Outline each uninfected red blood cell.
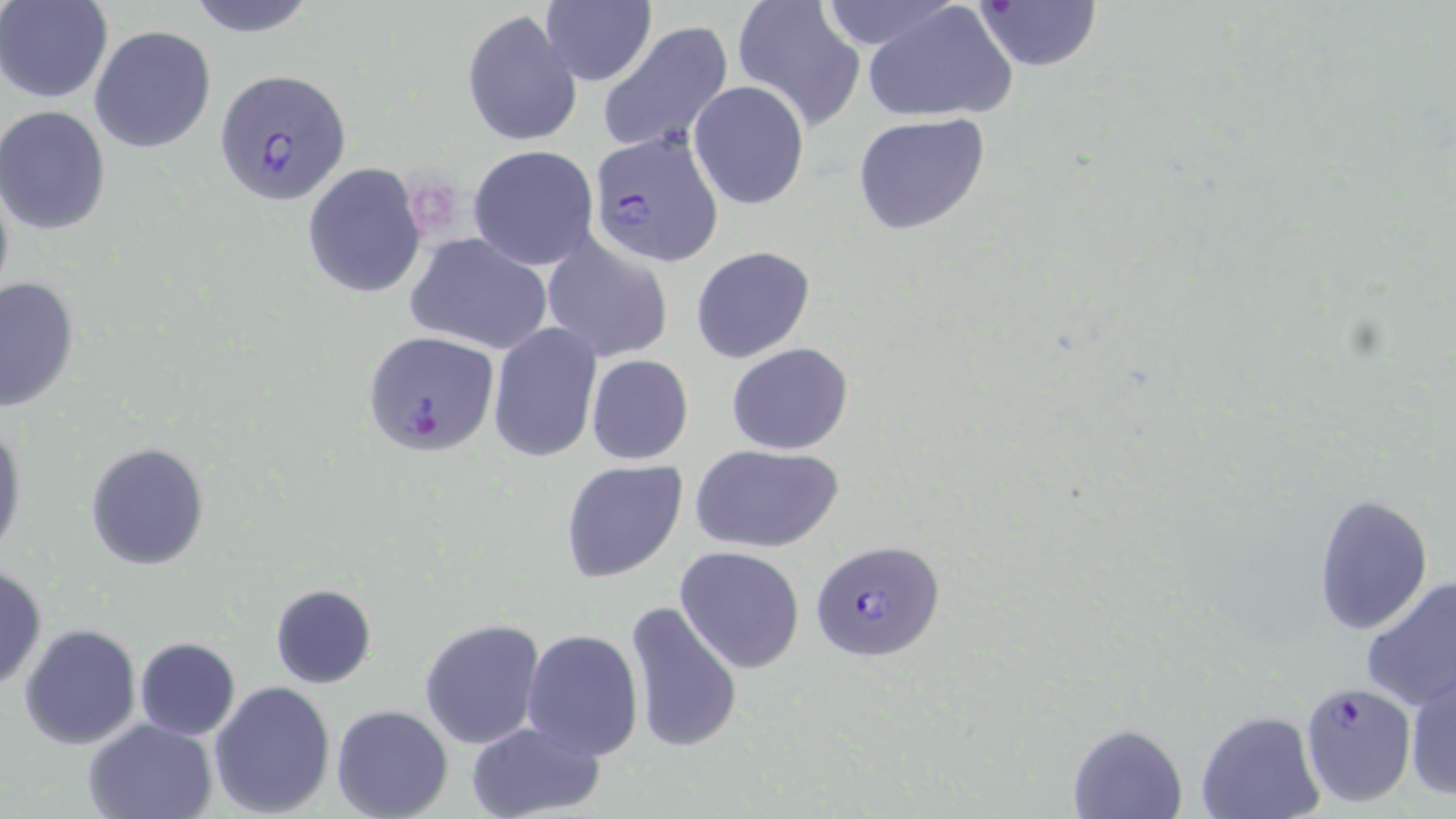

Approximate bounding boxes as (x1, y1, x2, y2) in pixels.
Uninfected red blood cells: (1, 0, 113, 102), (183, 0, 321, 36), (731, 0, 868, 131), (814, 0, 958, 50), (973, 0, 1101, 71), (541, 2, 657, 86), (863, 2, 1017, 124), (462, 9, 582, 147), (597, 20, 734, 155), (89, 25, 216, 154), (688, 80, 811, 211), (0, 105, 112, 236), (852, 113, 991, 237), (468, 145, 599, 270), (302, 163, 428, 297), (0, 167, 14, 314), (541, 232, 674, 362), (406, 233, 554, 354), (690, 246, 816, 363), (0, 275, 80, 414), (486, 322, 603, 463), (726, 341, 853, 456), (585, 354, 693, 465), (0, 414, 25, 564), (85, 442, 210, 571), (689, 442, 846, 553), (559, 458, 689, 582), (1312, 492, 1434, 636), (675, 546, 805, 673), (0, 563, 48, 692), (1359, 575, 1455, 714), (269, 583, 376, 688), (623, 600, 743, 754), (419, 618, 545, 750), (20, 624, 141, 749), (521, 627, 644, 759), (134, 637, 240, 740), (1405, 669, 1456, 800), (208, 680, 337, 816), (332, 704, 453, 819), (1195, 711, 1327, 819), (84, 718, 219, 818), (465, 720, 607, 818), (1067, 722, 1188, 819).

Summary:
  - Plasmodium falciparum-infected red blood cell locations: (212, 67, 352, 206), (588, 131, 724, 268), (361, 330, 499, 457), (811, 539, 944, 662), (1299, 682, 1418, 807)
  - Slide-level diagnosis: Plasmodium falciparum
  - Field of view: single
  - Stain: May-Grünwald-Giemsa
  - Modality: optical microscopy
  - Image size: 1456×819 pixels
  - Magnification: 1000x
  - Preparation: thin blood smear